Assess this cell for malaria.
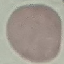

It is uninfected.

Thin smear of blood. Automatically extracted cell patch, resized to 64 × 64 pixels. Giemsa stain. Photographed with a smartphone camera at the microscope eyepiece.